Classify this cell by malaria status.
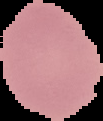
It is uninfected.

Image is 103×121 pixels. From a thin blood film. The area outside the segmented cell region is set to black.